Comment on the morphology of the erythrocytes.
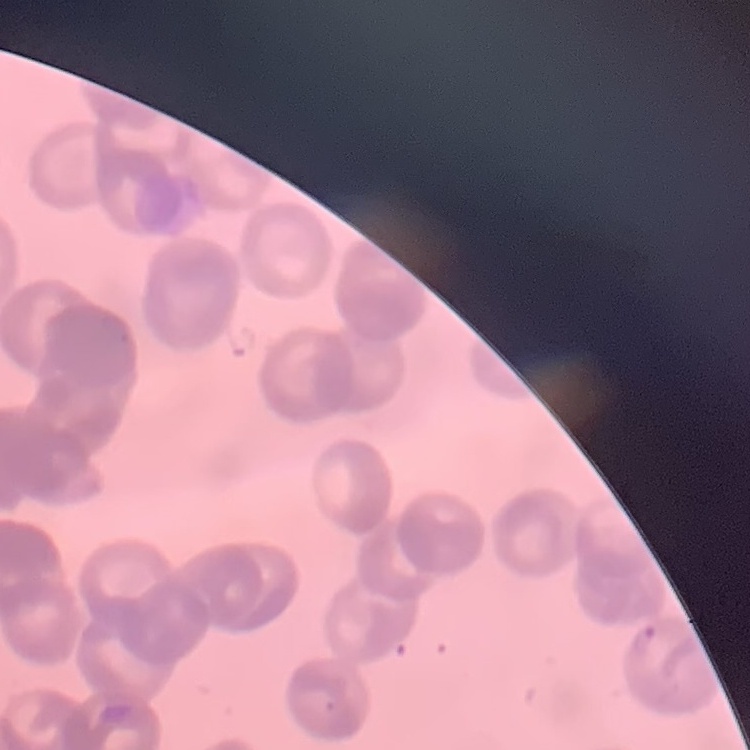
Rouleaux formation.

Thin peripheral smear. One tile cut from a larger photomicrograph. Field's or Giemsa stain.